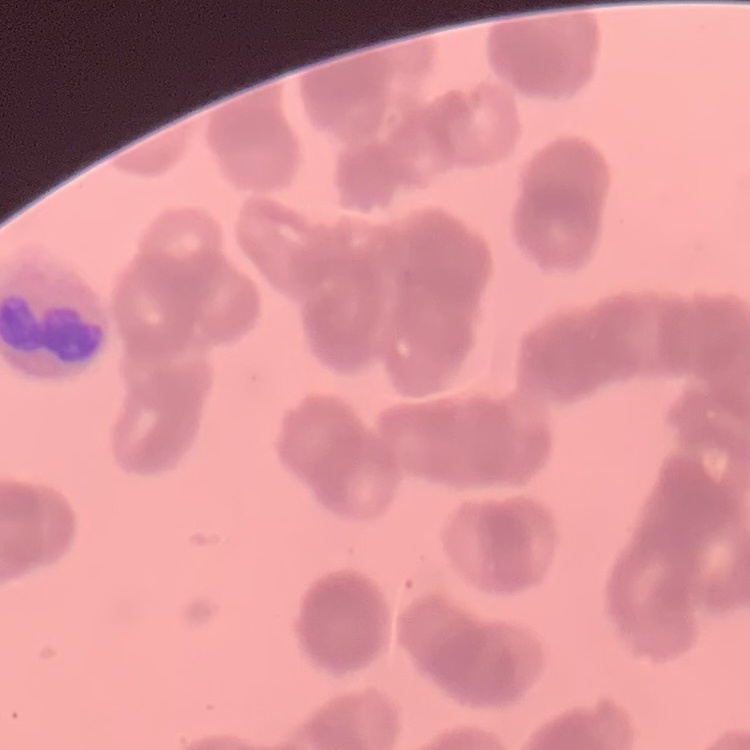

Summary:
  - Erythrocyte morphology: rouleaux formation
  - Stain: Field's or Giemsa
  - Image type: one tile cut from a larger photomicrograph
  - Preparation: thin blood smear